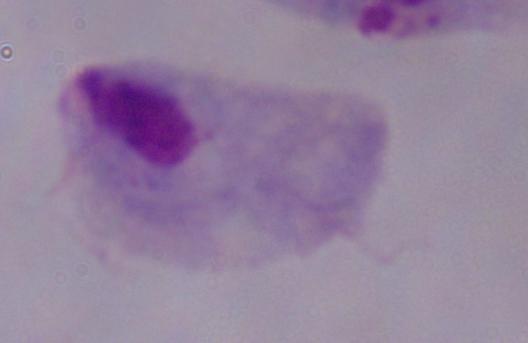
modality: photomicrograph
magnification: 1000x
identification: trichomonad